State the blood parasite species.
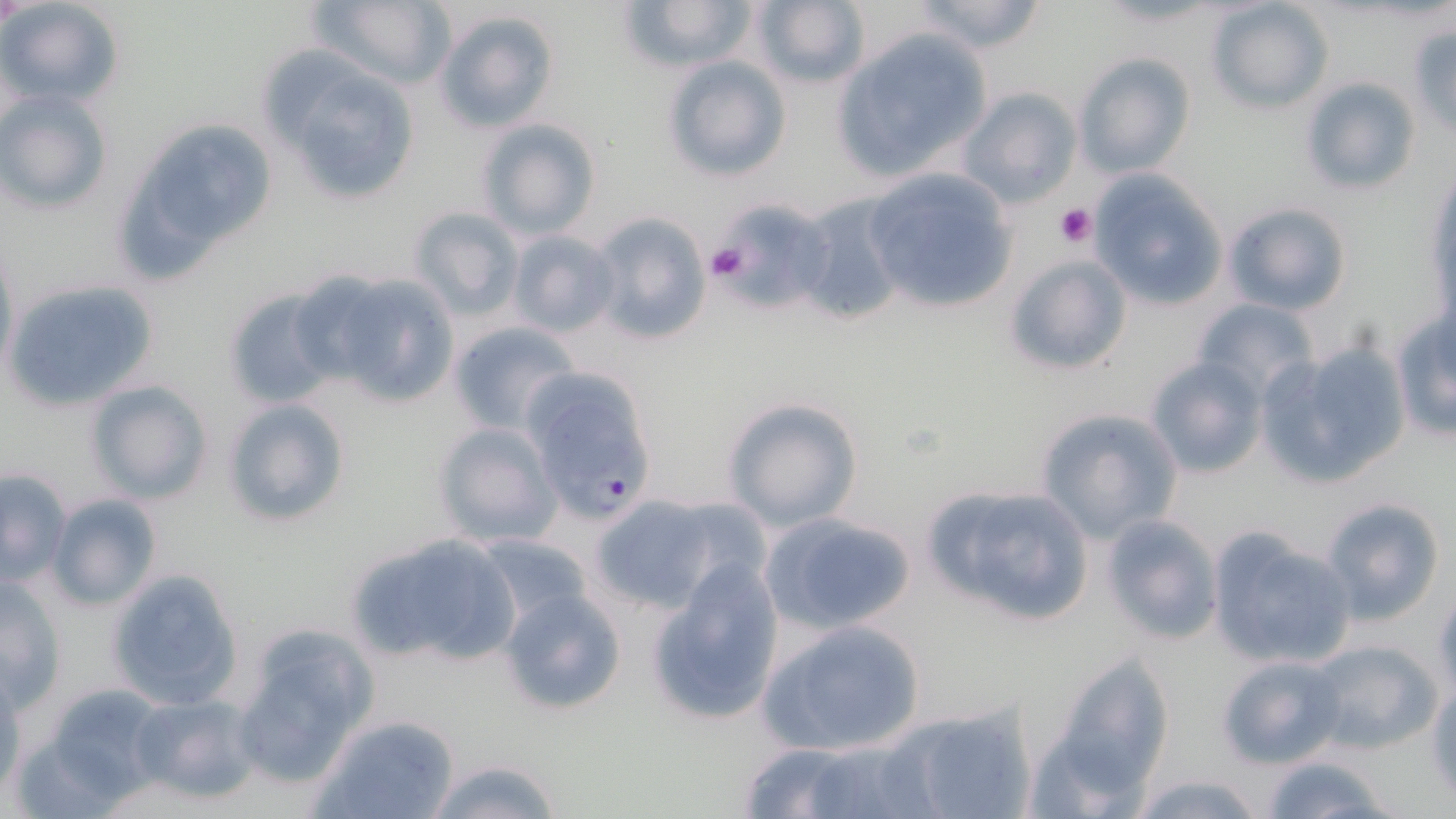

Plasmodium falciparum.

Approximate bounding boxes as (x1, y1, x2, y2) in pixels. Uninfected red blood cell locations: (0, 0, 124, 108), (313, 0, 454, 88), (619, 0, 759, 73), (752, 0, 869, 90), (905, 0, 1051, 53), (1206, 0, 1335, 113), (434, 8, 560, 134), (1406, 24, 1456, 136), (832, 26, 994, 183), (264, 52, 423, 207), (1073, 53, 1196, 180), (661, 56, 791, 182), (1302, 76, 1418, 195), (957, 87, 1083, 207), (1, 88, 112, 213), (159, 114, 268, 232), (475, 117, 600, 241), (863, 168, 1016, 314), (1086, 171, 1226, 310), (126, 173, 222, 286), (795, 196, 910, 329), (1223, 201, 1353, 315), (720, 204, 839, 316), (407, 206, 525, 322), (586, 211, 710, 345), (509, 231, 619, 337), (1003, 253, 1133, 377), (321, 272, 463, 409), (4, 277, 162, 412), (225, 288, 340, 410), (1192, 298, 1318, 400), (1390, 308, 1455, 440), (446, 321, 581, 435), (1263, 340, 1412, 484), (1145, 357, 1268, 478), (85, 380, 213, 505), (221, 396, 349, 528), (721, 397, 861, 532), (1035, 406, 1183, 543), (433, 422, 561, 548), (1, 469, 72, 584), (922, 484, 1096, 625), (45, 493, 160, 610), (589, 495, 734, 612), (1319, 496, 1445, 623), (758, 511, 918, 636), (1099, 514, 1224, 646), (1204, 527, 1356, 669), (346, 530, 520, 669), (474, 533, 592, 629), (647, 560, 787, 727), (105, 568, 244, 711), (1, 575, 67, 709), (501, 587, 626, 714), (758, 617, 927, 757), (230, 622, 377, 786), (1304, 638, 1444, 757), (1038, 645, 1177, 804), (1218, 653, 1349, 769), (1428, 682, 1456, 803), (31, 683, 172, 806), (133, 695, 260, 803), (890, 702, 1039, 819), (314, 713, 461, 819), (733, 740, 936, 819), (1259, 753, 1396, 819), (417, 758, 566, 819), (1127, 771, 1269, 819). Plasmodium falciparum-infected red blood cell locations: (517, 367, 659, 523). Platelet locations: (1055, 202, 1097, 248), (705, 241, 751, 284). Thin blood smear. May-Grünwald-Giemsa-stained preparation. 1000x magnification. One field of a larger specimen. Light microscopy. Image is 1456×819 pixels.